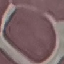

Summary:
  - Result: negative for malaria parasites
  - Capture: smartphone through the microscope eyepiece
  - Image type: cell patch, automatically extracted from a larger field of view and resized to 64 × 64 pixels
  - Preparation: thin smear
  - Stain: Giemsa